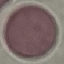

result = negative for malaria parasites
preparation = thin smear
image type = cell patch, automatically extracted from a larger field of view and resized to 64 × 64 pixels
stain = Giemsa
capture = smartphone camera at the microscope eyepiece